State which parasite is depicted.
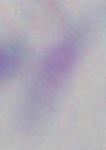
Toxoplasma gondii.

magnification = 1000x
modality = micrograph